Identify the parasite.
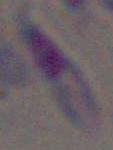
Toxoplasma gondii.

magnification = 1000x
modality = micrograph